Assess the morphology of the red blood cells.
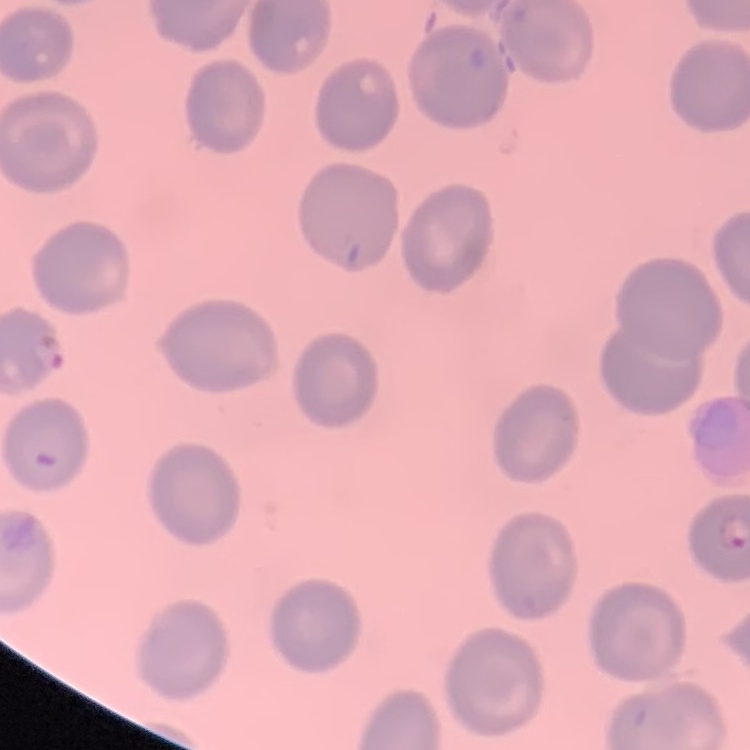

No rouleaux formation.

Summary:
  - Image type: one tile cut from a larger photomicrograph
  - Preparation: thin blood film
  - Stain: Field's or Giemsa